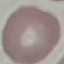
result = no malaria parasites detected
preparation = thin blood smear
stain = Giemsa
image type = automatically extracted cell patch, resized to 64 × 64 pixels
capture = smartphone through the microscope eyepiece